State which cell type is depicted.
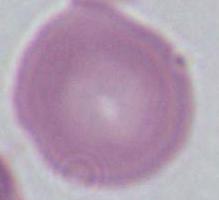

An erythrocyte.

Summary:
  - Modality: photomicrograph
  - Magnification: 1000x